Give the extent of all uninfected red blood cells.
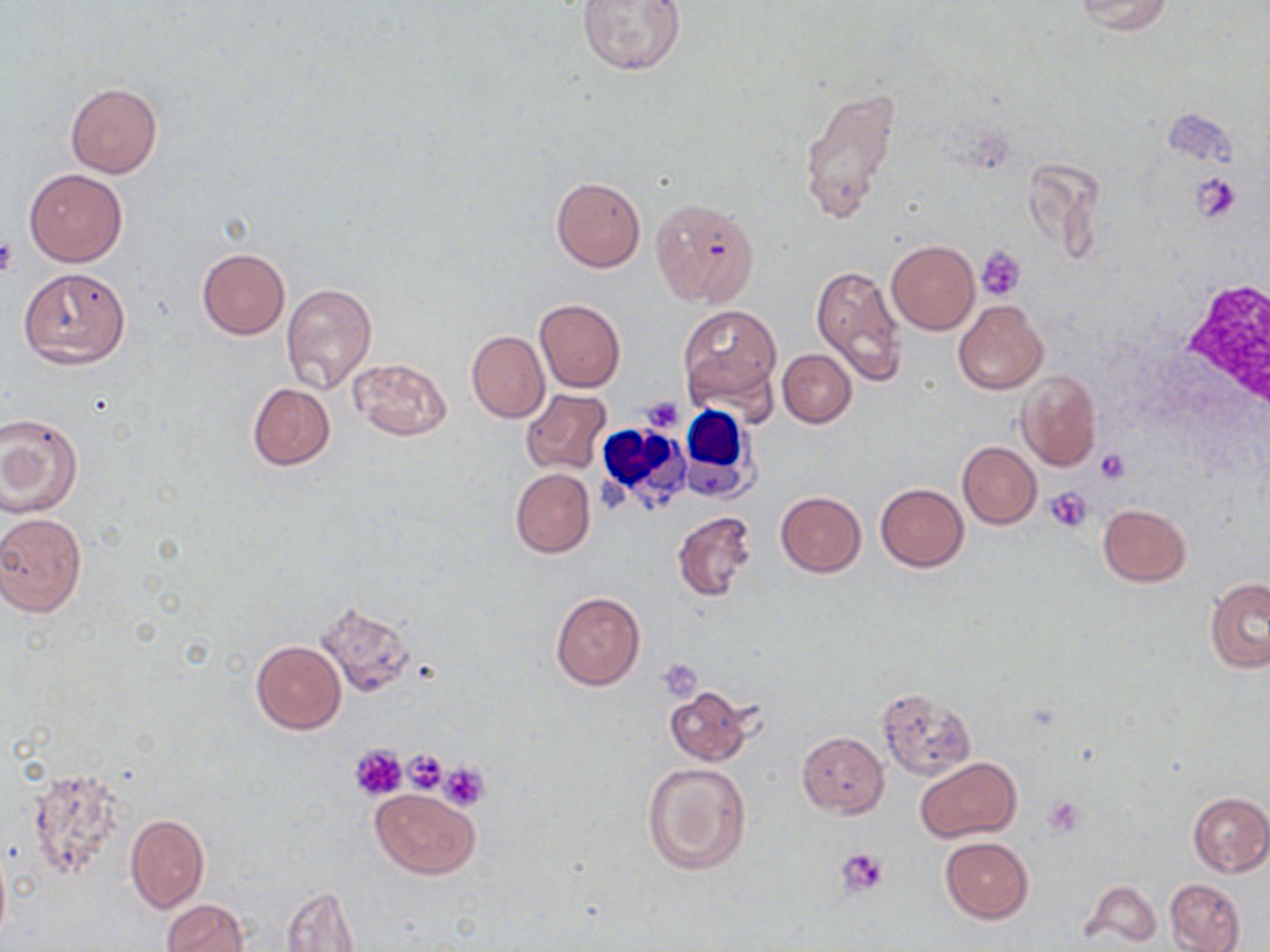

Approximate bounding boxes as named x1/y1/x2/y2 corners in pixels.
Uninfected red blood cells: (x1=577, y1=0, x2=686, y2=75), (x1=1073, y1=0, x2=1173, y2=34), (x1=66, y1=82, x2=161, y2=179), (x1=799, y1=85, x2=902, y2=225), (x1=1165, y1=108, x2=1237, y2=168), (x1=24, y1=169, x2=127, y2=266), (x1=551, y1=176, x2=646, y2=273), (x1=651, y1=198, x2=759, y2=308), (x1=885, y1=240, x2=979, y2=335), (x1=197, y1=247, x2=289, y2=340), (x1=811, y1=262, x2=907, y2=388), (x1=18, y1=266, x2=130, y2=368), (x1=282, y1=283, x2=377, y2=393), (x1=534, y1=299, x2=626, y2=392), (x1=953, y1=300, x2=1048, y2=394), (x1=679, y1=304, x2=779, y2=406), (x1=466, y1=331, x2=549, y2=423), (x1=777, y1=349, x2=855, y2=427), (x1=351, y1=357, x2=452, y2=440), (x1=1017, y1=370, x2=1101, y2=470), (x1=246, y1=383, x2=335, y2=470), (x1=520, y1=389, x2=612, y2=476), (x1=0, y1=412, x2=84, y2=517), (x1=957, y1=441, x2=1041, y2=529), (x1=510, y1=468, x2=594, y2=558), (x1=876, y1=484, x2=968, y2=571), (x1=774, y1=492, x2=866, y2=576), (x1=1098, y1=503, x2=1191, y2=586), (x1=672, y1=511, x2=756, y2=601), (x1=0, y1=512, x2=89, y2=617), (x1=1205, y1=578, x2=1270, y2=674), (x1=550, y1=590, x2=646, y2=691), (x1=316, y1=600, x2=417, y2=697), (x1=251, y1=640, x2=345, y2=734), (x1=664, y1=685, x2=752, y2=765), (x1=876, y1=688, x2=976, y2=779), (x1=797, y1=731, x2=889, y2=817), (x1=916, y1=756, x2=1020, y2=843), (x1=641, y1=760, x2=751, y2=877), (x1=27, y1=765, x2=127, y2=879), (x1=371, y1=787, x2=480, y2=879), (x1=1187, y1=791, x2=1270, y2=876), (x1=125, y1=813, x2=209, y2=912), (x1=940, y1=837, x2=1033, y2=923), (x1=0, y1=841, x2=11, y2=952), (x1=1164, y1=878, x2=1246, y2=952), (x1=1083, y1=882, x2=1159, y2=946), (x1=281, y1=886, x2=359, y2=951), (x1=160, y1=899, x2=248, y2=952).

{
  "slide_level_diagnosis": "negative for blood parasites",
  "white_blood_cell_locations": "approximate bounding boxes as named x1/y1/x2/y2 corners in pixels: (x1=677, y1=403, x2=757, y2=496), (x1=604, y1=428, x2=692, y2=504)",
  "preparation": "thin blood film",
  "stain": "May-Grünwald-Giemsa",
  "magnification": "1000x",
  "modality": "light microscopy",
  "image_size": "1270×952 pixels",
  "platelet_locations": "approximate bounding boxes as named x1/y1/x2/y2 corners in pixels: (x1=1193, y1=173, x2=1243, y2=224), (x1=0, y1=237, x2=18, y2=278), (x1=977, y1=245, x2=1025, y2=301), (x1=639, y1=396, x2=685, y2=436), (x1=1096, y1=447, x2=1132, y2=481), (x1=1045, y1=487, x2=1092, y2=531), (x1=658, y1=658, x2=705, y2=699), (x1=350, y1=744, x2=407, y2=801), (x1=401, y1=749, x2=448, y2=795), (x1=440, y1=761, x2=489, y2=809), (x1=1043, y1=796, x2=1085, y2=835), (x1=836, y1=845, x2=889, y2=897)",
  "field_of_view": "single"
}